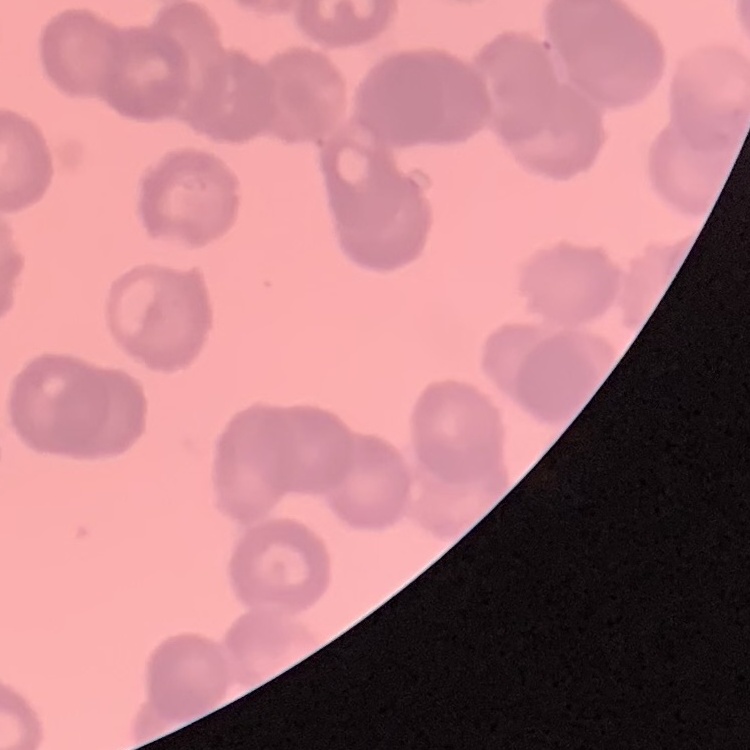 The erythrocytes show rouleaux formation. Stained with either Field's or Giemsa. Square crop of a larger photomicrograph. Thin blood smear.